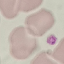
result = no malaria parasites detected
preparation = thin smear
image type = cell patch, automatically extracted from a larger field of view and resized to 64 × 64 pixels
capture = smartphone through the microscope eyepiece
stain = Giemsa